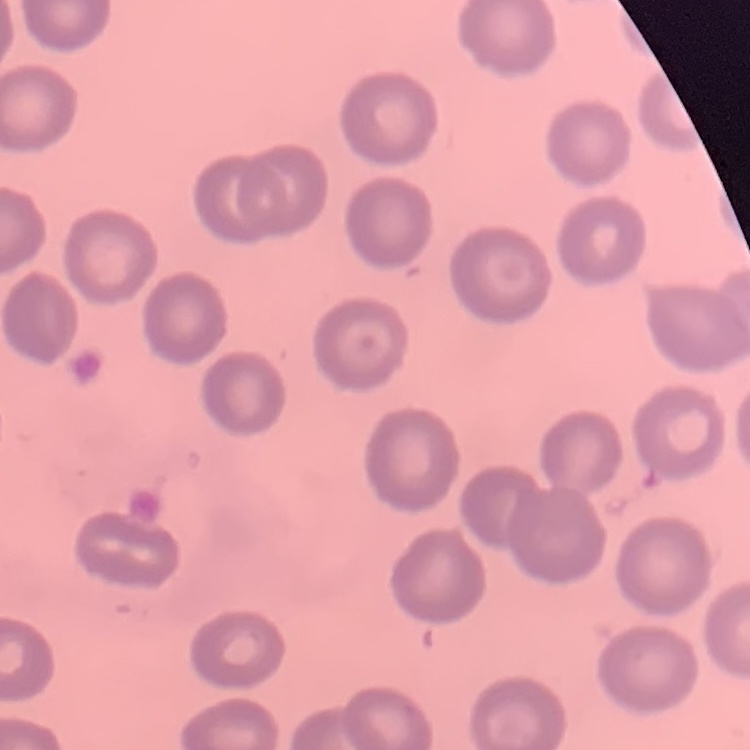

Summary:
  - Erythrocyte morphology: no rouleaux formation
  - Image type: square crop of a larger photomicrograph
  - Stain: Field's or Giemsa
  - Preparation: thin blood smear